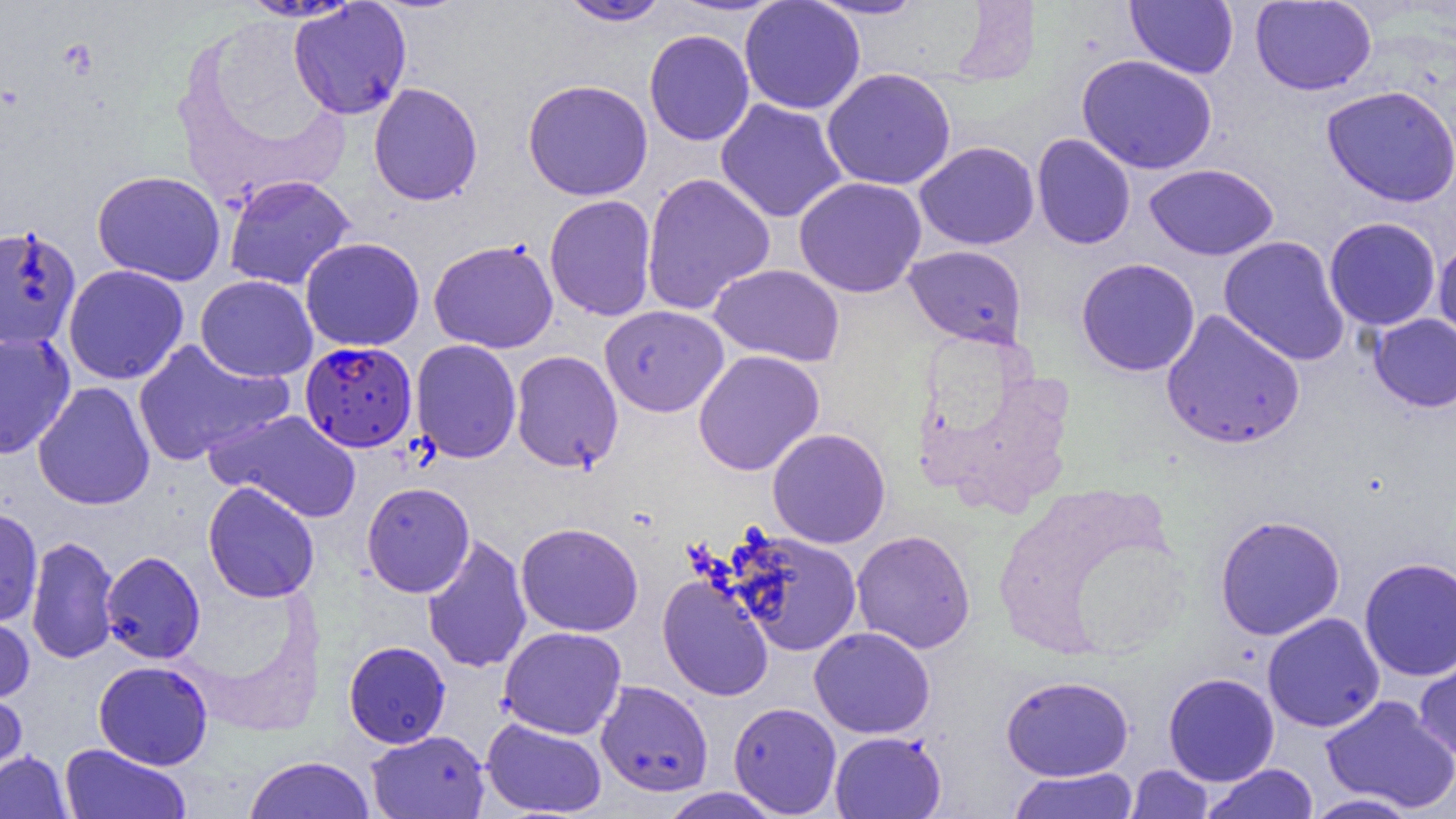

Approximate bounding boxes as named x1/y1/x2/y2 corners in pixels. Uninfected red blood cell locations: (x1=739, y1=0, x2=865, y2=115), (x1=806, y1=0, x2=927, y2=20), (x1=559, y1=1, x2=672, y2=26), (x1=1125, y1=1, x2=1239, y2=78), (x1=1249, y1=1, x2=1376, y2=95), (x1=289, y1=2, x2=412, y2=120), (x1=644, y1=29, x2=755, y2=146), (x1=1077, y1=54, x2=1217, y2=174), (x1=821, y1=67, x2=957, y2=191), (x1=522, y1=79, x2=653, y2=200), (x1=368, y1=82, x2=483, y2=206), (x1=1321, y1=85, x2=1456, y2=207), (x1=715, y1=99, x2=848, y2=223), (x1=1032, y1=133, x2=1136, y2=249), (x1=914, y1=141, x2=1040, y2=250), (x1=1144, y1=163, x2=1279, y2=261), (x1=92, y1=170, x2=226, y2=285), (x1=641, y1=172, x2=775, y2=314), (x1=224, y1=174, x2=356, y2=291), (x1=793, y1=176, x2=927, y2=298), (x1=544, y1=194, x2=657, y2=321), (x1=1324, y1=217, x2=1441, y2=331), (x1=0, y1=224, x2=82, y2=351), (x1=1218, y1=235, x2=1350, y2=366), (x1=300, y1=237, x2=425, y2=351), (x1=1434, y1=238, x2=1456, y2=349), (x1=428, y1=239, x2=559, y2=353), (x1=904, y1=244, x2=1027, y2=348), (x1=1076, y1=258, x2=1201, y2=376), (x1=709, y1=263, x2=846, y2=367), (x1=62, y1=264, x2=189, y2=385), (x1=195, y1=275, x2=318, y2=382), (x1=599, y1=305, x2=729, y2=417), (x1=1161, y1=309, x2=1305, y2=450), (x1=1369, y1=314, x2=1456, y2=412), (x1=0, y1=332, x2=75, y2=459), (x1=131, y1=339, x2=292, y2=466), (x1=410, y1=339, x2=522, y2=463), (x1=693, y1=349, x2=825, y2=476), (x1=510, y1=350, x2=623, y2=473), (x1=32, y1=381, x2=155, y2=510), (x1=205, y1=410, x2=361, y2=523), (x1=767, y1=427, x2=890, y2=549), (x1=203, y1=481, x2=320, y2=603), (x1=361, y1=481, x2=475, y2=597), (x1=0, y1=506, x2=43, y2=627), (x1=1215, y1=514, x2=1345, y2=640), (x1=516, y1=522, x2=644, y2=636), (x1=851, y1=529, x2=976, y2=654), (x1=730, y1=530, x2=863, y2=656), (x1=421, y1=534, x2=533, y2=674), (x1=26, y1=535, x2=119, y2=664), (x1=101, y1=551, x2=205, y2=664), (x1=1359, y1=556, x2=1456, y2=682), (x1=658, y1=574, x2=774, y2=701), (x1=0, y1=611, x2=35, y2=704), (x1=1262, y1=613, x2=1385, y2=732), (x1=498, y1=626, x2=627, y2=739), (x1=809, y1=626, x2=935, y2=739), (x1=343, y1=641, x2=451, y2=748), (x1=1414, y1=650, x2=1456, y2=764), (x1=93, y1=660, x2=213, y2=770), (x1=1163, y1=672, x2=1280, y2=786), (x1=1001, y1=675, x2=1134, y2=781), (x1=595, y1=680, x2=713, y2=796), (x1=0, y1=683, x2=28, y2=786), (x1=1320, y1=694, x2=1456, y2=813), (x1=728, y1=701, x2=842, y2=817), (x1=481, y1=718, x2=607, y2=817), (x1=366, y1=730, x2=490, y2=818), (x1=830, y1=731, x2=947, y2=819), (x1=59, y1=743, x2=192, y2=818), (x1=0, y1=750, x2=72, y2=819), (x1=243, y1=755, x2=375, y2=818), (x1=1200, y1=763, x2=1319, y2=819), (x1=1126, y1=764, x2=1213, y2=818), (x1=1008, y1=767, x2=1139, y2=819), (x1=658, y1=788, x2=784, y2=818), (x1=1303, y1=793, x2=1421, y2=818). Plasmodium falciparum-infected red blood cell locations: (x1=300, y1=344, x2=418, y2=456). Slide-level diagnosis: Plasmodium falciparum. One field of a larger specimen. Image is 1456×819 pixels. Light microscopy. Thin blood film. 1000x magnification.